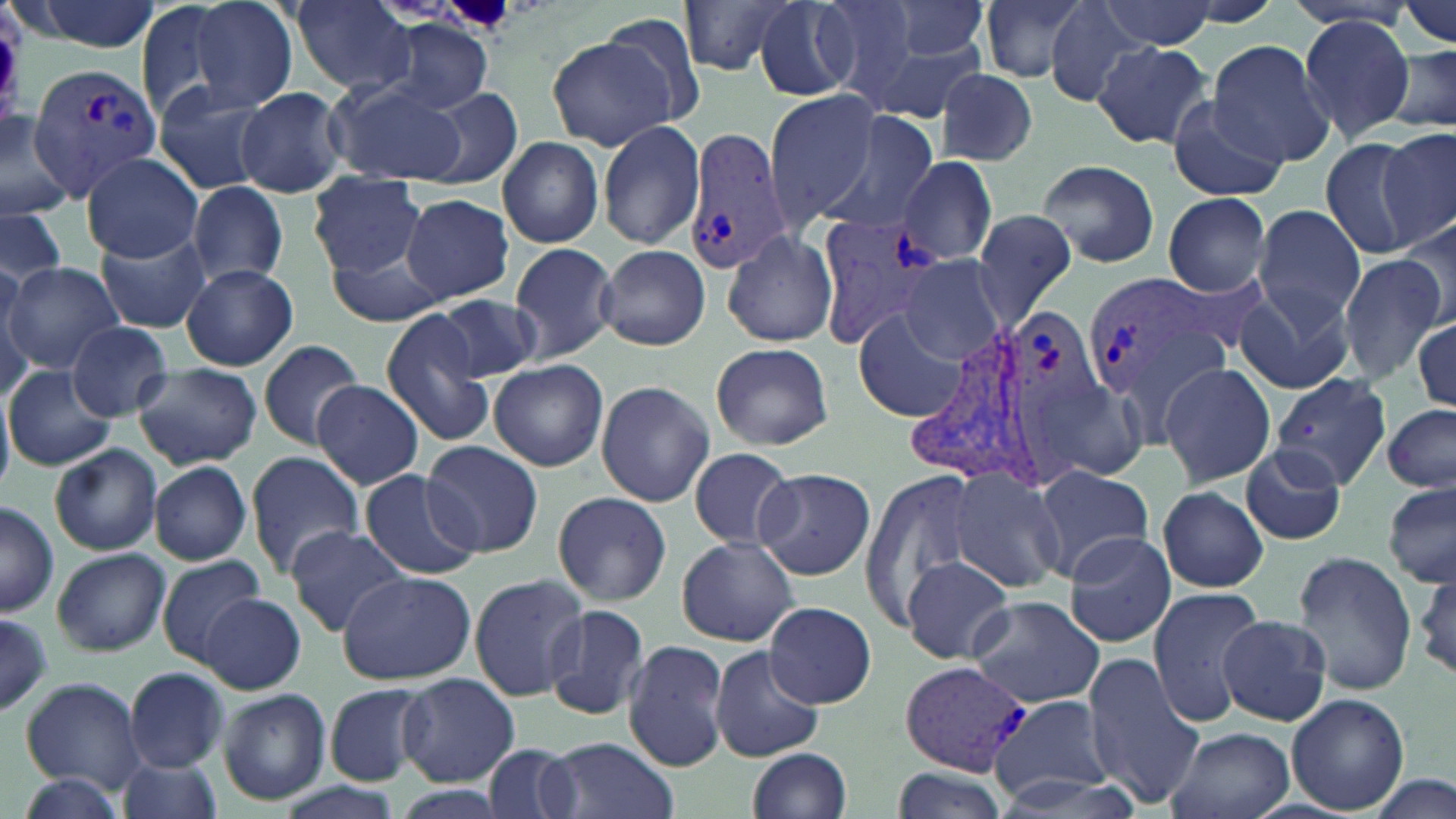

Summary:
  - Coordinate format: approximate bounding boxes as (x1, y1, x2, y2) in pixels
  - Plasmodium vivax-infected red blood cell locations: (26, 62, 167, 197), (685, 126, 794, 276), (819, 214, 951, 350), (1081, 270, 1222, 402), (1005, 307, 1105, 490), (906, 325, 1044, 482), (897, 659, 1037, 775)
  - Uninfected red blood cell locations: (22, 0, 163, 52), (176, 0, 301, 115), (290, 0, 414, 94), (677, 0, 799, 77), (812, 0, 920, 104), (883, 0, 991, 65), (979, 0, 1096, 86), (753, 1, 860, 99), (1045, 1, 1154, 106), (1101, 1, 1217, 51), (1395, 1, 1456, 51), (588, 14, 709, 133), (1296, 16, 1415, 141), (378, 17, 494, 117), (547, 35, 679, 152), (864, 38, 987, 124), (1204, 40, 1335, 169), (1093, 41, 1214, 149), (1385, 44, 1456, 136), (935, 67, 1039, 168), (327, 79, 468, 186), (153, 82, 275, 195), (237, 86, 348, 199), (421, 88, 522, 190), (764, 90, 882, 225), (1168, 100, 1285, 201), (0, 104, 81, 223), (818, 111, 942, 235), (597, 119, 705, 250), (1376, 129, 1453, 248), (497, 136, 605, 248), (1318, 136, 1423, 259), (82, 152, 204, 262), (899, 155, 997, 265), (1038, 159, 1159, 269), (307, 174, 426, 276), (188, 181, 289, 287), (1163, 192, 1272, 296), (400, 194, 513, 305), (970, 205, 1079, 327), (1252, 205, 1366, 330), (0, 207, 68, 288), (1399, 215, 1455, 326), (98, 228, 209, 333), (721, 228, 838, 348), (510, 242, 618, 362), (596, 244, 710, 350), (327, 253, 446, 322), (1337, 254, 1448, 385), (902, 257, 1007, 363), (3, 261, 127, 376), (0, 263, 36, 388), (182, 264, 297, 371), (1236, 285, 1357, 396), (437, 295, 541, 382), (380, 307, 497, 447), (853, 311, 965, 422), (1413, 316, 1454, 410), (65, 322, 173, 419), (258, 339, 365, 449), (709, 342, 834, 451), (489, 358, 609, 471), (1158, 361, 1276, 488), (132, 364, 261, 469), (5, 365, 115, 471), (1271, 371, 1392, 488), (1030, 372, 1154, 488), (313, 380, 424, 490), (595, 381, 716, 507), (0, 392, 15, 493), (1381, 405, 1456, 494), (422, 440, 543, 557), (49, 444, 161, 555), (1240, 445, 1348, 546), (688, 447, 796, 550), (245, 451, 366, 576), (149, 461, 252, 565), (1030, 465, 1153, 572), (753, 466, 876, 580), (949, 466, 1070, 591), (360, 468, 482, 581), (859, 469, 986, 623), (1383, 479, 1456, 589), (1157, 485, 1269, 593), (552, 490, 671, 606), (0, 503, 59, 617), (284, 524, 409, 636), (1061, 531, 1175, 647), (675, 537, 801, 646), (50, 546, 170, 657), (1292, 551, 1419, 695), (156, 554, 266, 665), (901, 555, 1015, 665), (1412, 562, 1454, 687), (337, 571, 475, 683), (468, 573, 591, 703), (1148, 587, 1268, 726), (201, 592, 307, 694), (968, 595, 1104, 709), (764, 601, 876, 708), (541, 603, 651, 720), (0, 614, 56, 714), (1218, 615, 1333, 725), (622, 639, 729, 770), (708, 645, 827, 762), (1082, 654, 1205, 808), (124, 667, 228, 771), (398, 672, 519, 786), (20, 677, 146, 793), (325, 684, 429, 785), (218, 689, 332, 806), (1287, 692, 1411, 814), (989, 694, 1117, 802), (1165, 726, 1294, 819), (543, 735, 678, 819), (483, 740, 583, 819), (747, 747, 852, 819), (114, 754, 223, 819), (891, 765, 1014, 819), (984, 771, 1148, 818), (12, 772, 133, 819), (1369, 774, 1453, 819), (276, 782, 402, 819)
  - Slide-level diagnosis: Plasmodium vivax
  - Field of view: single
  - Image size: 1456×819 pixels
  - Modality: light microscopy
  - Preparation: thin blood film
  - Stain: May-Grünwald-Giemsa
  - Magnification: 1000x